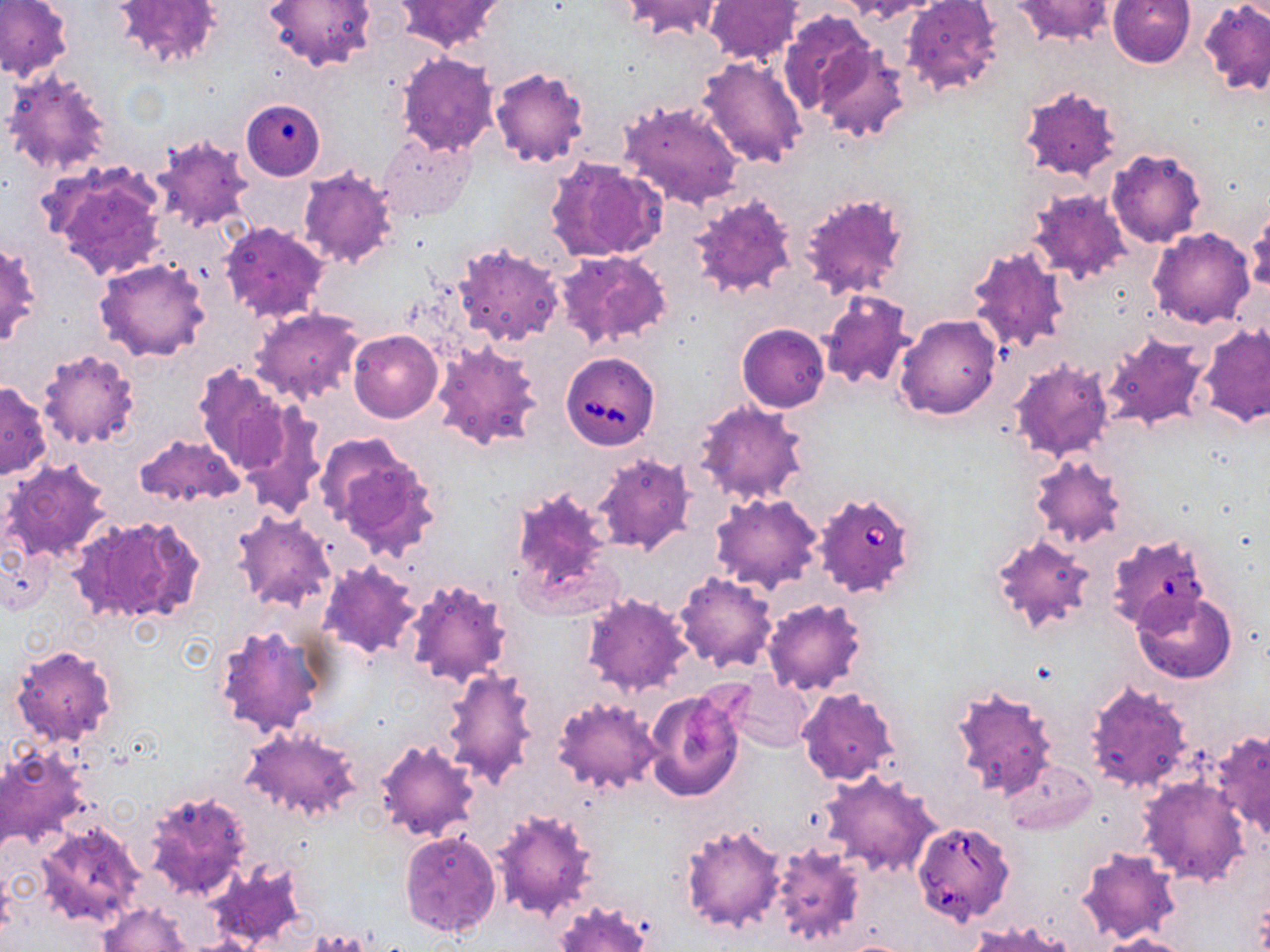

Approximate bounding boxes as named x1/y1/x2/y2 corners in pixels. Babesia divergens-infected red blood cell locations: (x1=560, y1=352, x2=659, y2=449), (x1=814, y1=491, x2=919, y2=598), (x1=1107, y1=533, x2=1209, y2=634), (x1=910, y1=820, x2=1015, y2=926). Uninfected red blood cell locations: (x1=0, y1=0, x2=72, y2=81), (x1=113, y1=0, x2=223, y2=69), (x1=265, y1=0, x2=376, y2=73), (x1=620, y1=0, x2=726, y2=41), (x1=847, y1=0, x2=944, y2=21), (x1=901, y1=0, x2=1004, y2=99), (x1=1012, y1=0, x2=1117, y2=45), (x1=396, y1=1, x2=505, y2=53), (x1=704, y1=1, x2=803, y2=64), (x1=1108, y1=1, x2=1195, y2=69), (x1=1200, y1=1, x2=1270, y2=94), (x1=780, y1=11, x2=873, y2=117), (x1=813, y1=44, x2=913, y2=145), (x1=395, y1=53, x2=500, y2=157), (x1=696, y1=53, x2=808, y2=166), (x1=488, y1=67, x2=589, y2=169), (x1=4, y1=68, x2=111, y2=177), (x1=1017, y1=84, x2=1122, y2=179), (x1=618, y1=99, x2=746, y2=210), (x1=240, y1=100, x2=321, y2=181), (x1=377, y1=133, x2=475, y2=221), (x1=149, y1=135, x2=253, y2=231), (x1=1107, y1=149, x2=1205, y2=247), (x1=544, y1=156, x2=667, y2=263), (x1=46, y1=164, x2=168, y2=281), (x1=295, y1=165, x2=398, y2=269), (x1=1027, y1=186, x2=1132, y2=284), (x1=796, y1=192, x2=910, y2=301), (x1=689, y1=194, x2=798, y2=301), (x1=1246, y1=213, x2=1270, y2=296), (x1=218, y1=222, x2=331, y2=325), (x1=1148, y1=228, x2=1254, y2=329), (x1=0, y1=239, x2=39, y2=346), (x1=452, y1=241, x2=565, y2=348), (x1=967, y1=243, x2=1071, y2=355), (x1=555, y1=250, x2=671, y2=350), (x1=94, y1=258, x2=212, y2=362), (x1=818, y1=289, x2=915, y2=391), (x1=250, y1=306, x2=364, y2=406), (x1=895, y1=315, x2=1001, y2=420), (x1=737, y1=322, x2=829, y2=413), (x1=1196, y1=324, x2=1270, y2=428), (x1=348, y1=330, x2=443, y2=423), (x1=1101, y1=332, x2=1212, y2=430), (x1=432, y1=338, x2=543, y2=452), (x1=37, y1=349, x2=141, y2=450), (x1=1009, y1=360, x2=1114, y2=461), (x1=194, y1=363, x2=294, y2=476), (x1=1, y1=381, x2=51, y2=479), (x1=693, y1=400, x2=808, y2=505), (x1=240, y1=409, x2=327, y2=517), (x1=317, y1=434, x2=442, y2=561), (x1=133, y1=435, x2=242, y2=509), (x1=591, y1=453, x2=696, y2=555), (x1=1027, y1=454, x2=1128, y2=550), (x1=3, y1=458, x2=113, y2=564), (x1=507, y1=483, x2=616, y2=615), (x1=710, y1=492, x2=824, y2=595), (x1=230, y1=511, x2=336, y2=613), (x1=73, y1=514, x2=206, y2=627), (x1=991, y1=534, x2=1097, y2=636), (x1=0, y1=543, x2=56, y2=614), (x1=317, y1=561, x2=422, y2=660), (x1=675, y1=573, x2=778, y2=673), (x1=403, y1=578, x2=514, y2=688), (x1=1131, y1=590, x2=1237, y2=684), (x1=581, y1=593, x2=694, y2=698), (x1=762, y1=597, x2=868, y2=695), (x1=213, y1=620, x2=331, y2=739), (x1=9, y1=642, x2=118, y2=748), (x1=441, y1=667, x2=540, y2=788), (x1=726, y1=673, x2=812, y2=752), (x1=1083, y1=680, x2=1193, y2=795), (x1=950, y1=684, x2=1057, y2=801), (x1=797, y1=686, x2=899, y2=786), (x1=643, y1=687, x2=745, y2=801), (x1=550, y1=694, x2=662, y2=795), (x1=241, y1=727, x2=362, y2=822), (x1=1210, y1=728, x2=1270, y2=840), (x1=374, y1=740, x2=480, y2=842), (x1=0, y1=744, x2=92, y2=853), (x1=1004, y1=758, x2=1096, y2=835), (x1=819, y1=770, x2=942, y2=878), (x1=1138, y1=777, x2=1249, y2=886), (x1=142, y1=790, x2=252, y2=900), (x1=491, y1=807, x2=600, y2=922), (x1=34, y1=820, x2=145, y2=927), (x1=679, y1=821, x2=788, y2=935), (x1=400, y1=830, x2=502, y2=938), (x1=769, y1=844, x2=864, y2=947), (x1=1078, y1=848, x2=1181, y2=944), (x1=207, y1=859, x2=308, y2=948), (x1=554, y1=901, x2=652, y2=952), (x1=99, y1=902, x2=194, y2=951), (x1=971, y1=921, x2=1076, y2=952), (x1=1103, y1=933, x2=1197, y2=952). Slide-level diagnosis: Babesia divergens. Image is 1270×952 pixels. Thin blood smear. May-Grünwald-Giemsa stain. Single field of view. Optical microscopy. 1000x magnification.